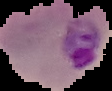

Cell region segmented out of the field of view; the surrounding area is masked to black. Result: malaria parasites detected. Image is 112×91 pixels. From a thin blood film.